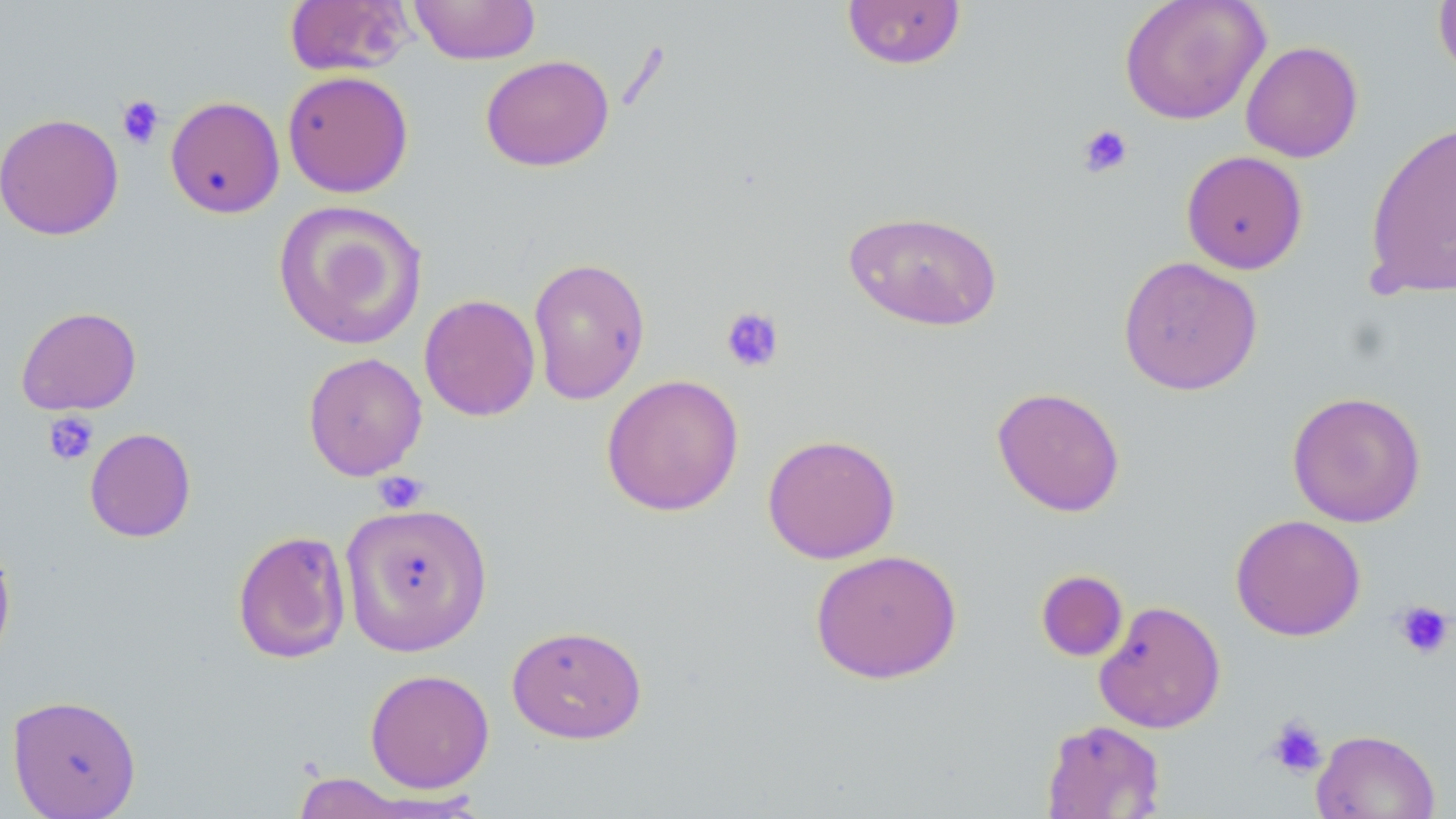 Approximate bounding boxes as (x1, y1, x2, y2) in pixels. Uninfected red blood cell locations: (283, 0, 414, 76), (408, 0, 541, 65), (840, 0, 967, 70), (1119, 0, 1271, 124), (1433, 0, 1456, 83), (1240, 41, 1363, 162), (480, 54, 614, 172), (282, 70, 414, 198), (165, 95, 285, 219), (0, 112, 124, 240), (1363, 120, 1455, 301), (1181, 150, 1308, 274), (272, 199, 428, 351), (843, 209, 1004, 331), (1117, 255, 1263, 396), (527, 257, 651, 404), (419, 294, 541, 421), (15, 306, 142, 416), (302, 352, 427, 480), (600, 374, 744, 516), (991, 386, 1126, 517), (1287, 390, 1426, 528), (84, 427, 196, 543), (762, 433, 901, 564), (339, 502, 493, 656), (1230, 514, 1366, 641), (231, 530, 351, 664), (0, 534, 16, 668), (809, 548, 963, 684), (1036, 569, 1128, 662), (1093, 599, 1227, 734), (506, 624, 647, 744), (364, 668, 495, 794), (7, 694, 141, 818), (1041, 718, 1166, 818), (1311, 729, 1440, 819), (288, 772, 424, 818). Platelet locations: (116, 94, 165, 150), (1078, 124, 1133, 179), (720, 306, 785, 373), (43, 412, 99, 465), (372, 470, 429, 514), (1392, 600, 1454, 659), (1265, 716, 1327, 778). Slide-level diagnosis: negative for blood parasites. Thin blood film. May-Grünwald-Giemsa-stained preparation. One field of a larger specimen. Image is 1456×819 pixels. Light microscopy. 1000x magnification.